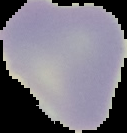
Summary:
  - Preparation: thin blood film
  - Result: negative for malaria parasites
  - Image size: 127×133 pixels
  - Image type: cell region segmented out of the field of view; surrounding area masked to black